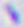

identification = Toxoplasma gondii
modality = micrograph
magnification = 400x